Report the malaria status of this cell.
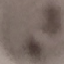

Uninfected.

Summary:
  - Stain: Giemsa
  - Image type: cell patch, automatically extracted from a larger field of view and resized to 64 × 64 pixels
  - Preparation: thin smear
  - Capture: smartphone camera at the microscope eyepiece